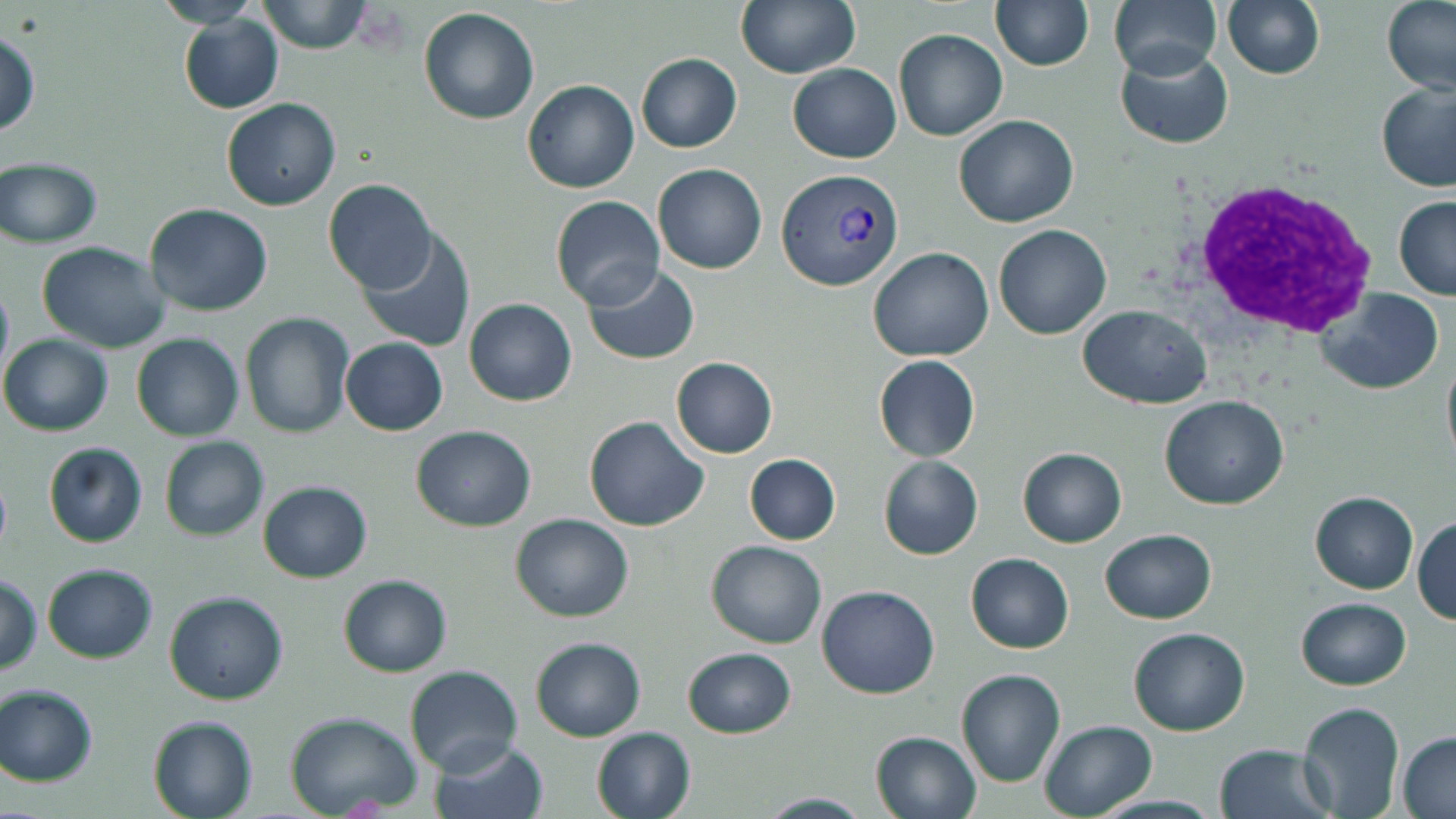 Approximate bounding boxes as [x1, y1, x2, y2] in pixels. White blood cell locations: [1183, 176, 1375, 340]. Plasmodium vivax-infected red blood cell locations: [779, 168, 905, 290]. Uninfected red blood cell locations: [257, 0, 374, 54], [735, 0, 858, 78], [991, 0, 1093, 70], [1110, 0, 1222, 77], [1222, 0, 1326, 80], [1381, 0, 1456, 97], [418, 8, 540, 125], [181, 14, 285, 114], [0, 28, 40, 137], [895, 28, 1007, 142], [1115, 45, 1235, 149], [635, 53, 741, 152], [788, 64, 902, 163], [522, 79, 639, 194], [1377, 81, 1456, 193], [221, 97, 342, 211], [952, 114, 1079, 227], [0, 158, 103, 249], [652, 164, 767, 275], [6, 170, 119, 316], [322, 179, 438, 294], [551, 196, 665, 308], [1393, 196, 1456, 301], [144, 203, 273, 316], [992, 223, 1111, 339], [357, 228, 477, 353], [36, 241, 171, 351], [868, 246, 994, 362], [582, 263, 700, 366], [0, 276, 13, 389], [1319, 288, 1445, 395], [464, 298, 576, 406], [1078, 304, 1212, 409], [240, 312, 358, 440], [1, 334, 115, 436], [131, 334, 243, 441], [340, 337, 447, 436], [1441, 347, 1456, 474], [671, 356, 778, 458], [873, 356, 980, 462], [1160, 395, 1289, 510], [583, 415, 710, 532], [410, 425, 536, 531], [159, 435, 268, 541], [43, 442, 147, 548], [1018, 447, 1126, 548], [743, 454, 840, 546], [878, 455, 983, 560], [257, 481, 373, 583], [1310, 491, 1418, 593], [509, 512, 634, 622], [1412, 516, 1456, 625], [1100, 530, 1216, 623], [706, 539, 827, 650], [965, 552, 1074, 654], [43, 564, 158, 663], [1, 572, 43, 675], [337, 573, 453, 677], [817, 586, 940, 698], [163, 591, 289, 706], [1296, 598, 1410, 690], [1129, 627, 1250, 736], [531, 636, 645, 741], [683, 647, 795, 739], [405, 665, 524, 775], [956, 668, 1065, 788], [0, 684, 99, 786], [1298, 701, 1404, 818], [285, 711, 423, 818], [147, 715, 259, 819], [1039, 719, 1157, 819], [589, 726, 695, 819], [870, 730, 981, 818], [1397, 732, 1456, 817], [428, 736, 548, 819], [1214, 743, 1335, 819], [750, 792, 876, 818]. Slide-level diagnosis: Plasmodium vivax. Thin blood film. May-Grünwald-Giemsa stain. One field of a larger specimen. Image is 1456×819 pixels. Optical microscopy. 1000x magnification.